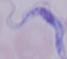

identification: trypanosome
modality: micrograph
magnification: 1000x